State the blood parasite species.
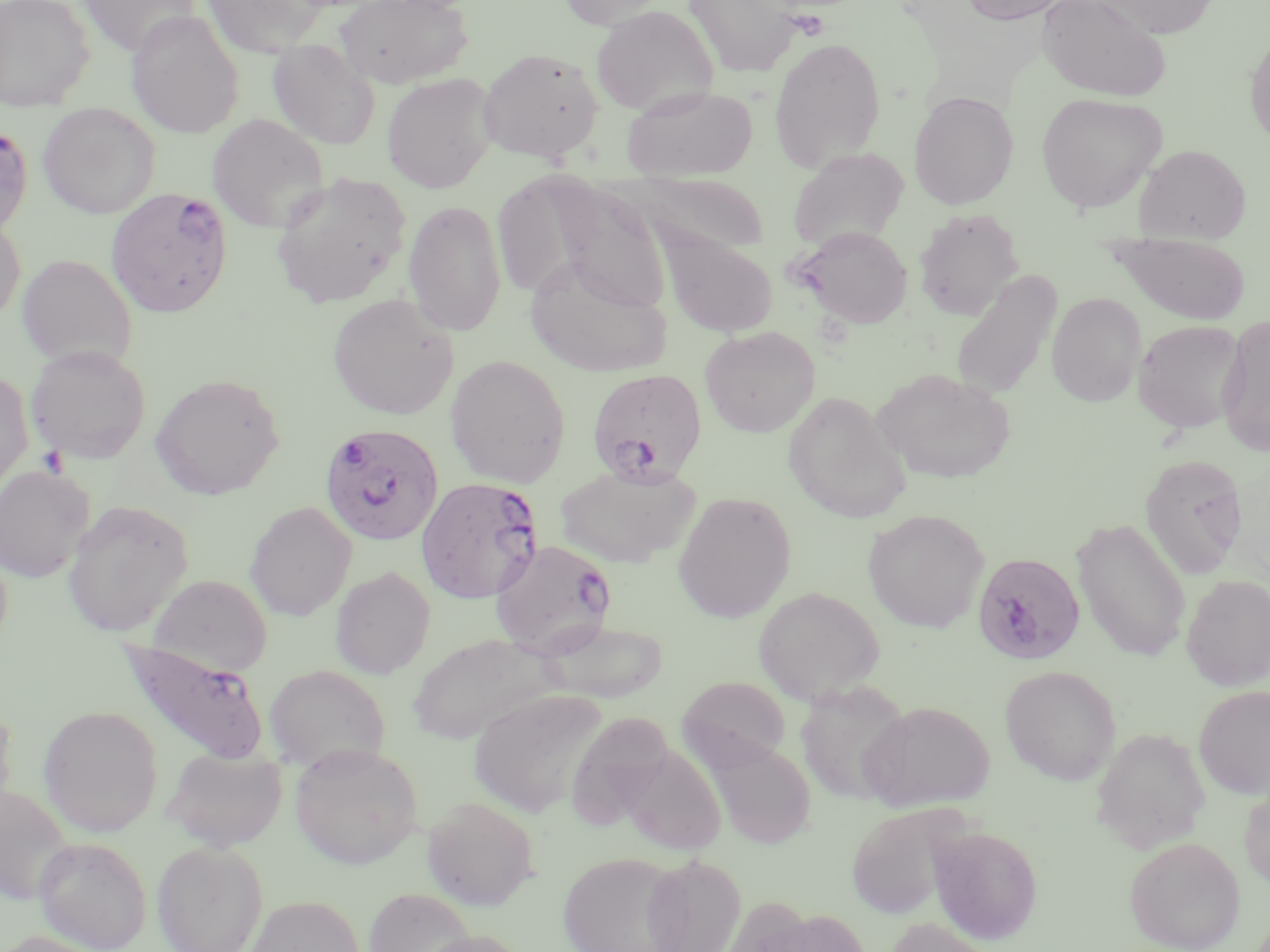

Plasmodium falciparum.

platelet locations = approximate bounding boxes as (x1,y1)-(x2,y2) corner pairs in pixels: (38,445)-(69,477)
modality = optical microscopy
Plasmodium falciparum-infected red blood cell locations = approximate bounding boxes as (x1,y1)-(x2,y2) corner pairs in pixels: (0,123)-(33,239), (106,186)-(232,318), (586,368)-(707,487), (318,422)-(444,547), (415,476)-(544,605), (490,539)-(617,659), (972,552)-(1086,671), (117,638)-(271,767)
field of view = single
stain = May-Grünwald-Giemsa
preparation = thin blood film
magnification = 1000x
image size = 1270×952 pixels
uninfected red blood cell locations = approximate bounding boxes as (x1,y1)-(x2,y2) corner pairs in pixels: (0,0)-(95,112), (78,0)-(203,57), (201,0)-(330,57), (334,0)-(473,89), (556,0)-(672,28), (683,0)-(804,76), (958,0)-(1074,25), (1037,0)-(1172,102), (1092,0)-(1218,38), (590,5)-(718,116), (127,9)-(245,139), (1244,30)-(1270,149), (768,36)-(886,172), (268,39)-(381,150), (478,47)-(604,163), (381,72)-(499,193), (622,85)-(759,180), (909,90)-(1019,209), (1036,92)-(1167,214), (38,103)-(160,218), (207,113)-(329,233), (1135,144)-(1251,244), (787,148)-(910,252), (269,172)-(411,308), (624,173)-(769,257), (549,182)-(673,315), (403,199)-(506,337), (913,208)-(1024,321), (0,216)-(25,326), (795,226)-(913,329), (1109,233)-(1252,325), (662,234)-(780,338), (17,254)-(137,370), (525,255)-(672,378), (949,270)-(1062,401), (1047,292)-(1146,407), (327,293)-(459,420), (1216,314)-(1270,457), (1133,319)-(1247,433), (699,326)-(820,437), (27,344)-(151,463), (446,355)-(571,488), (0,367)-(33,497), (873,368)-(1017,485), (150,373)-(285,500), (783,391)-(910,523), (1139,453)-(1249,580), (554,463)-(701,568), (0,465)-(94,582), (672,491)-(796,623), (62,500)-(193,638), (244,501)-(357,621), (863,509)-(989,632), (1071,517)-(1191,663), (330,566)-(436,679), (149,573)-(273,675), (1182,575)-(1270,691), (753,585)-(885,705), (540,618)-(669,703), (406,632)-(559,743), (264,664)-(391,773), (1000,665)-(1122,785), (677,676)-(790,770), (795,679)-(913,806), (1193,685)-(1270,800), (468,688)-(608,816), (0,699)-(17,827), (859,700)-(995,811), (38,705)-(163,836), (566,712)-(674,829), (1091,727)-(1211,853), (705,739)-(816,848), (620,742)-(726,856), (289,743)-(423,869), (163,747)-(287,851), (1239,775)-(1270,892), (1,784)-(75,905), (422,796)-(539,910), (846,802)-(966,921), (928,825)-(1043,945), (34,836)-(151,951), (1124,836)-(1245,952), (152,839)-(267,952), (557,851)-(689,952), (642,853)-(746,952), (364,886)-(477,951), (244,895)-(364,952), (746,907)-(868,952), (881,917)-(998,952), (413,930)-(531,952), (0,931)-(111,952)